Locate and identify every blood parasite.
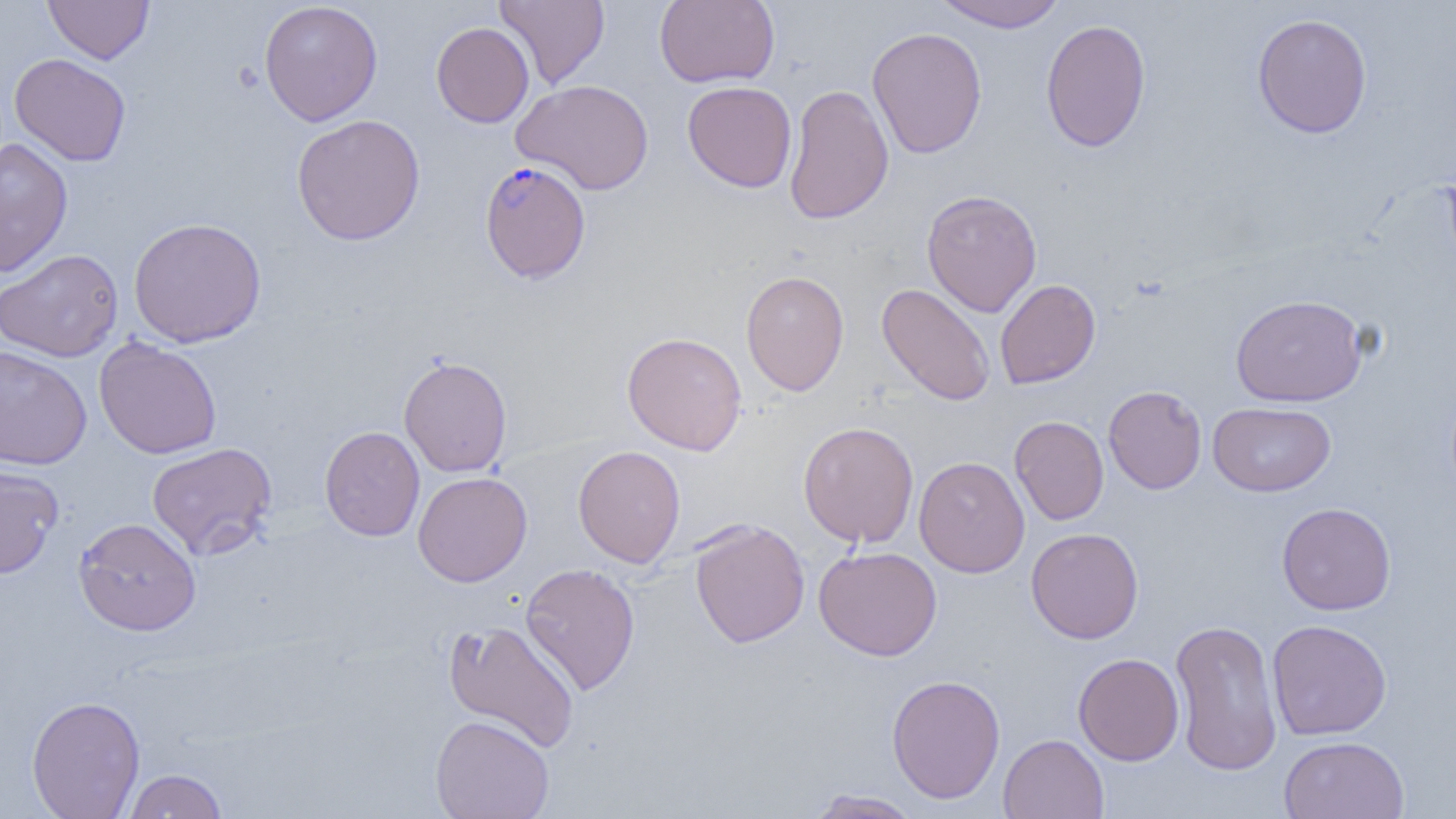

Approximate bounding boxes as (x1, y1, x2, y2) in pixels.
Plasmodium falciparum-infected red blood cells: (479, 160, 592, 284).
No Plasmodium ovale, Plasmodium malariae, Plasmodium vivax, Babesia divergens, or Trypanosoma brucei observed.

slide-level diagnosis = Plasmodium falciparum
field of view = single
modality = light microscopy
magnification = 1000x
uninfected red blood cell locations = approximate bounding boxes as (x1, y1, x2, y2) in pixels: (43, 0, 153, 64), (495, 0, 610, 89), (654, 0, 780, 88), (931, 0, 1069, 31), (258, 1, 383, 126), (1252, 13, 1372, 139), (1040, 18, 1151, 153), (431, 21, 534, 128), (866, 27, 987, 159), (9, 53, 131, 167), (512, 78, 655, 195), (682, 81, 797, 192), (784, 83, 894, 224), (291, 114, 426, 246), (0, 136, 73, 278), (921, 189, 1042, 317), (128, 217, 267, 347), (0, 248, 124, 362), (740, 270, 850, 396), (995, 279, 1101, 389), (877, 283, 996, 406), (1231, 293, 1368, 407), (622, 331, 747, 455), (94, 337, 222, 459), (0, 344, 92, 470), (399, 355, 512, 477), (1103, 385, 1207, 494), (1208, 402, 1336, 497), (1009, 415, 1109, 525), (1019, 415, 1115, 643), (798, 421, 919, 547), (319, 426, 425, 541), (147, 442, 278, 560), (572, 445, 686, 568), (914, 456, 1030, 578), (0, 465, 63, 579), (413, 471, 532, 587), (1277, 502, 1396, 615), (74, 517, 201, 635), (689, 519, 810, 648), (1026, 527, 1144, 644), (813, 545, 942, 661), (520, 563, 640, 695), (1169, 618, 1283, 777), (443, 620, 581, 752), (1267, 620, 1392, 741), (1073, 652, 1184, 765), (886, 674, 1005, 803), (26, 695, 145, 819), (430, 714, 555, 819), (998, 734, 1109, 819), (1278, 735, 1410, 819), (123, 769, 228, 818), (806, 789, 923, 819)
preparation = thin blood film
image size = 1456×819 pixels